Outline each blood parasite and name the species.
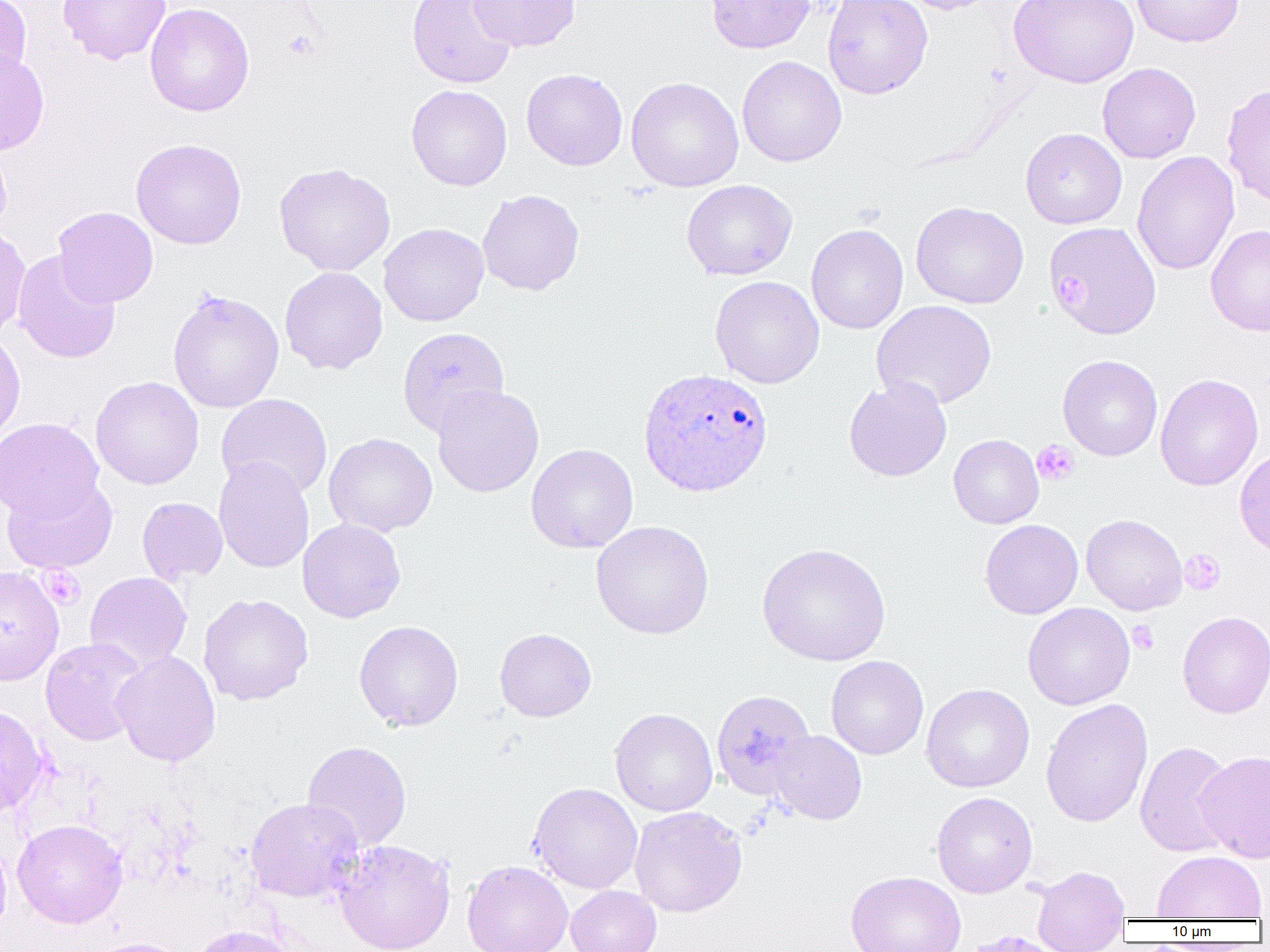
Approximate bounding boxes as (x1,y1)-(x2,y2) corner pairs in pixels.
Plasmodium ovale-infected red blood cells: (638,367)-(774,497).
No Plasmodium falciparum, Plasmodium malariae, Plasmodium vivax, Babesia divergens, or Trypanosoma brucei observed.

Uninfected red blood cell locations: (0,0)-(32,86), (58,0)-(170,65), (406,0)-(518,90), (470,0)-(580,52), (705,0)-(815,54), (821,0)-(933,99), (891,0)-(1003,14), (1131,0)-(1244,47), (1009,1)-(1139,88), (144,3)-(254,117), (0,49)-(49,155), (737,55)-(847,167), (1097,62)-(1201,164), (521,68)-(628,171), (625,76)-(744,192), (1221,83)-(1270,208), (406,84)-(512,191), (1020,128)-(1127,229), (131,138)-(247,249), (0,141)-(12,240), (1131,151)-(1240,275), (274,162)-(396,276), (681,179)-(797,281), (477,189)-(585,296), (911,201)-(1029,308), (52,206)-(158,307), (1044,221)-(1162,340), (379,223)-(489,326), (805,224)-(908,334), (1206,224)-(1270,336), (0,225)-(31,339), (12,251)-(121,364), (279,266)-(388,374), (710,276)-(824,388), (167,289)-(284,413), (871,300)-(996,410), (397,327)-(510,437), (0,329)-(26,446), (1057,355)-(1162,461), (1154,373)-(1264,491), (90,376)-(204,489), (843,377)-(952,482), (432,384)-(544,498), (216,393)-(333,500), (0,418)-(104,521), (324,432)-(438,537), (948,434)-(1043,529), (526,444)-(638,553), (1234,447)-(1270,559), (213,457)-(314,573), (2,475)-(118,574), (137,497)-(228,584), (1081,514)-(1187,615), (298,518)-(406,623), (980,519)-(1083,619), (591,521)-(714,639), (756,542)-(891,667), (0,565)-(64,686), (84,572)-(192,673), (199,593)-(313,705), (1023,602)-(1135,710), (1177,611)-(1270,718), (354,620)-(463,731), (495,628)-(597,722), (40,637)-(149,746), (112,650)-(220,766), (826,656)-(928,759), (921,683)-(1034,793), (712,690)-(815,799), (1040,698)-(1153,828), (0,705)-(48,819), (610,708)-(718,816), (768,730)-(867,824), (302,741)-(411,853), (1135,741)-(1236,858), (1195,750)-(1270,863), (529,782)-(642,893), (931,792)-(1037,898), (245,798)-(363,902), (630,806)-(747,917), (12,819)-(128,928), (0,834)-(12,941), (335,839)-(455,952), (1152,850)-(1266,921), (463,861)-(573,952), (1031,865)-(1130,952), (845,871)-(966,952), (566,885)-(661,952), (190,924)-(297,952), (88,937)-(195,952). Platelet locations: (283,30)-(319,60), (1058,275)-(1091,314), (1032,440)-(1079,486), (1180,549)-(1225,595), (40,566)-(86,610), (1128,620)-(1159,655). Slide-level diagnosis: Plasmodium ovale. Thin blood smear. One field of a larger specimen. Image is 1270×952 pixels. Optical microscopy. Captured at 1000x magnification.